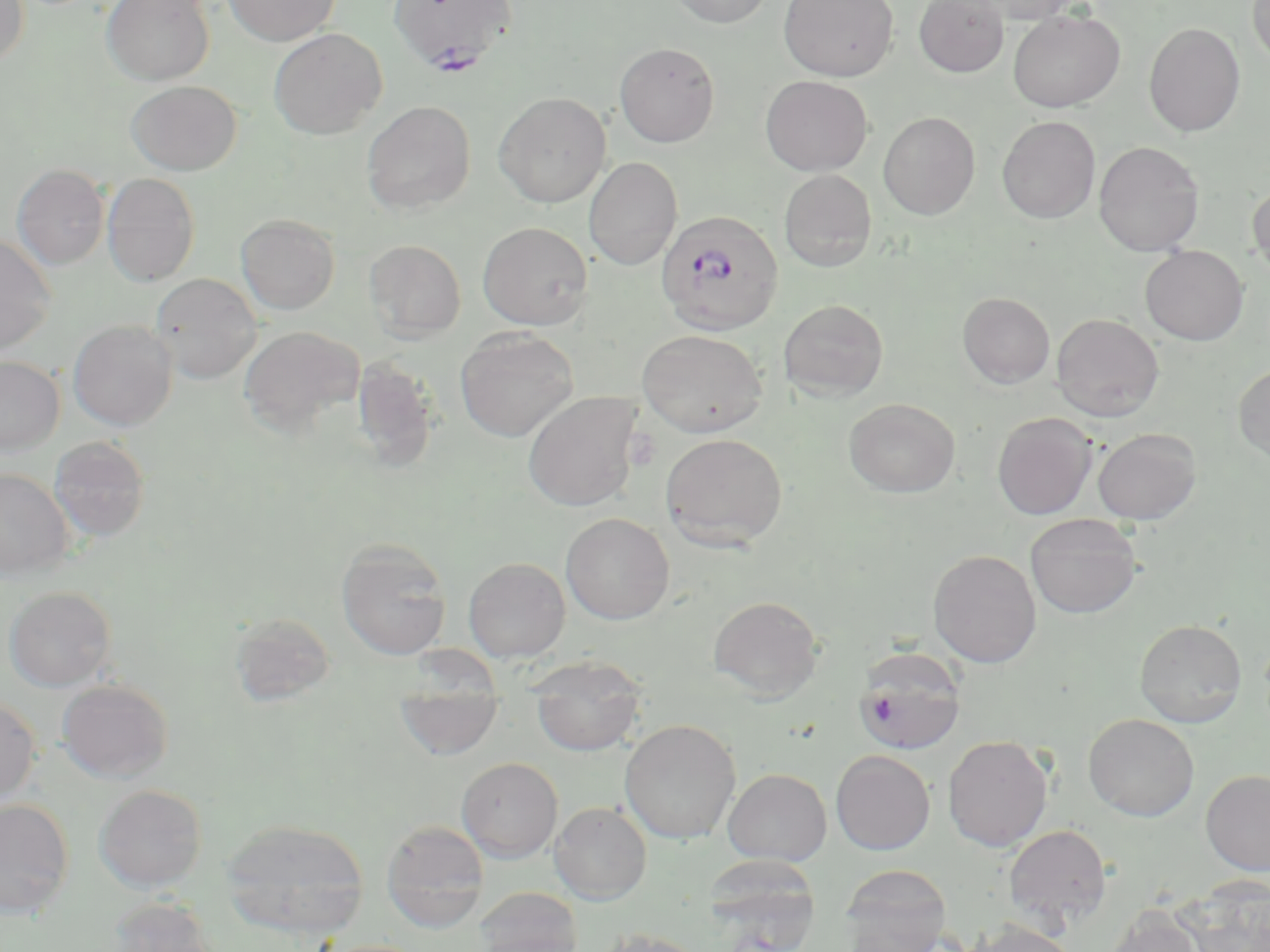 Approximate bounding boxes as [x1, y1, x2, y2] in pixels. Plasmodium falciparum-infected red blood cell locations: [388, 0, 517, 73], [656, 210, 784, 336]. Uninfected red blood cell locations: [0, 0, 30, 69], [102, 0, 215, 86], [224, 0, 340, 46], [668, 0, 774, 28], [778, 0, 898, 81], [914, 0, 1009, 77], [963, 0, 1086, 24], [1247, 0, 1270, 68], [1007, 9, 1125, 112], [1144, 22, 1246, 137], [268, 28, 388, 139], [614, 42, 720, 147], [760, 75, 872, 176], [126, 80, 241, 175], [493, 92, 611, 207], [361, 101, 476, 214], [878, 111, 980, 220], [997, 116, 1101, 223], [1093, 140, 1205, 256], [583, 157, 682, 270], [12, 164, 109, 269], [779, 169, 877, 272], [101, 173, 200, 287], [1247, 181, 1270, 283], [236, 213, 340, 315], [477, 221, 593, 330], [0, 234, 57, 354], [364, 239, 467, 341], [1140, 246, 1248, 345], [150, 272, 262, 383], [957, 292, 1055, 389], [778, 299, 889, 401], [1051, 313, 1164, 421], [68, 319, 177, 429], [239, 325, 365, 436], [454, 328, 579, 442], [637, 329, 768, 438], [350, 355, 441, 472], [0, 356, 65, 454], [1233, 363, 1270, 463], [522, 392, 642, 512], [844, 398, 960, 498], [992, 412, 1097, 519], [1092, 428, 1201, 525], [660, 432, 788, 550], [49, 436, 150, 542], [0, 468, 74, 580], [560, 513, 675, 625], [1024, 513, 1142, 619], [336, 537, 451, 660], [928, 549, 1042, 667], [463, 557, 570, 661], [3, 585, 116, 691], [708, 596, 823, 701], [230, 612, 337, 706], [1134, 618, 1247, 727], [853, 647, 967, 755], [521, 657, 647, 699], [56, 679, 173, 783], [0, 696, 40, 803], [532, 697, 643, 756], [395, 700, 504, 759], [1083, 712, 1200, 821], [619, 719, 741, 845], [942, 735, 1053, 852], [831, 750, 935, 855], [457, 757, 562, 863], [723, 768, 832, 866], [1200, 769, 1270, 875], [94, 784, 207, 892], [0, 799, 75, 919], [550, 802, 651, 905], [220, 819, 370, 938], [381, 820, 490, 933], [1003, 825, 1112, 929], [704, 857, 822, 951], [839, 864, 952, 952], [1181, 876, 1270, 952], [474, 886, 584, 952], [108, 896, 219, 952], [1104, 906, 1206, 952], [964, 919, 1079, 952], [594, 928, 709, 952], [315, 939, 430, 952]. Slide-level diagnosis: Plasmodium falciparum. Single field of view. Image is 1270×952 pixels. Thin blood film. Light microscopy. 1000x magnification. May-Grünwald-Giemsa-stained preparation.